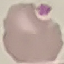
result = no malaria parasites detected
image type = cell patch, automatically extracted from a larger field of view and resized to 64 × 64 pixels
capture = smartphone camera at the microscope eyepiece
preparation = thin blood smear
stain = Giemsa